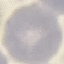
Summary:
  - Result: no malaria parasites seen
  - Preparation: thin blood film
  - Image type: automatically extracted cell patch, resized to 64 × 64 pixels
  - Capture: smartphone camera at the microscope eyepiece
  - Stain: Giemsa